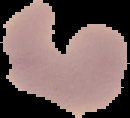
Summary:
  - Result: negative for Plasmodium parasites
  - Image size: 130×118 pixels
  - Image type: segmented cell region with the area outside set to black
  - Preparation: thin blood smear